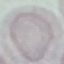

result = no malaria parasites detected
preparation = thin blood smear
capture = smartphone through the microscope eyepiece
stain = Giemsa
image type = automatically extracted cell patch, resized to 64 × 64 pixels